Outline each Plasmodium ovale-infected red blood cell.
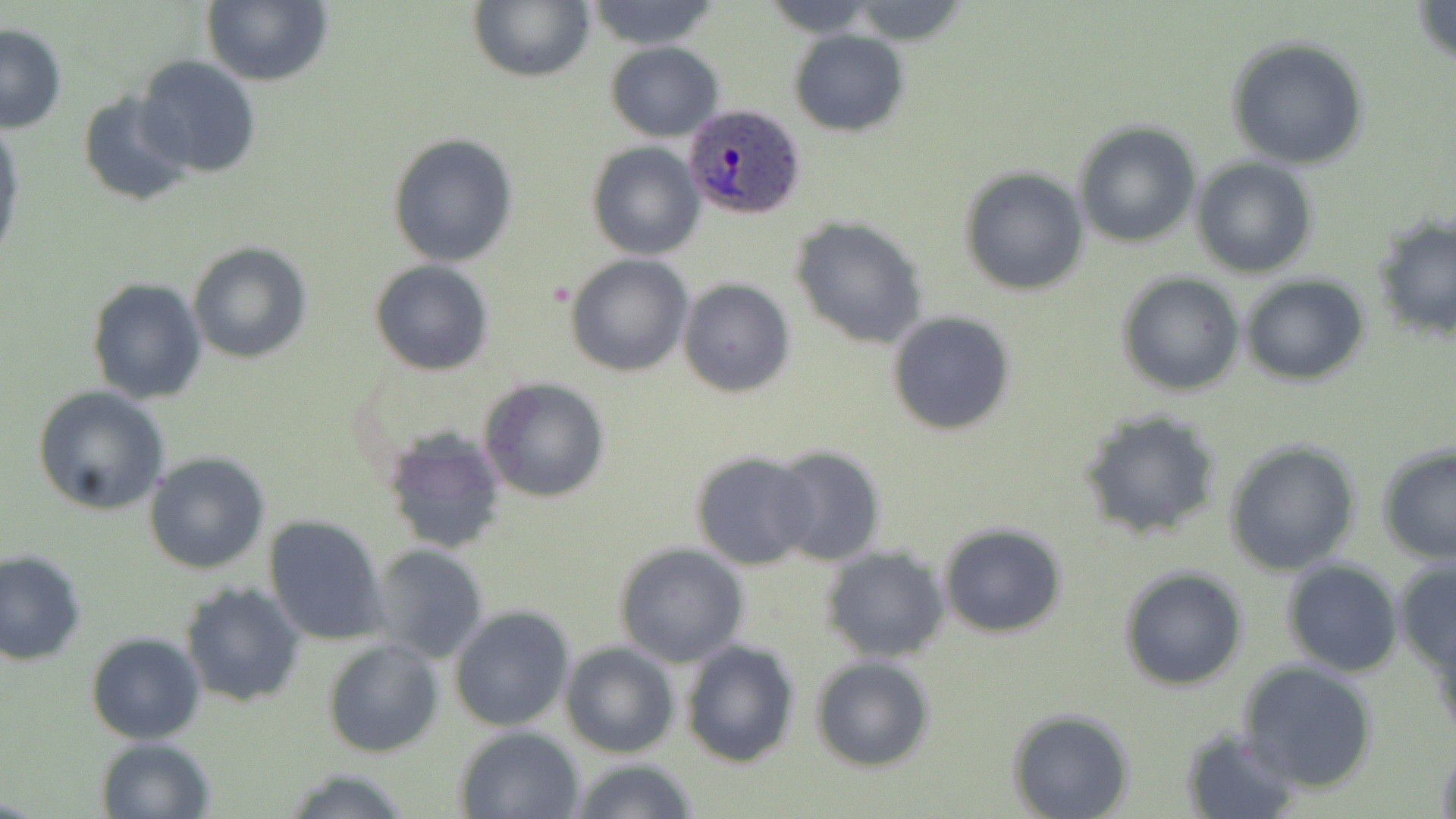
Approximate bounding boxes as [x1, y1, x2, y2] in pixels.
Plasmodium ovale-infected red blood cells: [681, 104, 808, 222].

Summary:
  - Uninfected red blood cell locations: [202, 0, 332, 88], [467, 1, 594, 83], [584, 1, 720, 50], [843, 1, 970, 45], [1412, 1, 1456, 67], [0, 22, 68, 132], [789, 30, 909, 136], [1225, 37, 1369, 170], [606, 41, 725, 141], [134, 55, 262, 178], [78, 90, 196, 207], [0, 121, 24, 266], [1073, 121, 1201, 248], [388, 133, 518, 267], [587, 142, 705, 259], [1192, 158, 1317, 278], [959, 166, 1091, 296], [1371, 212, 1456, 340], [790, 215, 927, 349], [188, 242, 312, 365], [565, 255, 692, 375], [370, 260, 493, 375], [1116, 272, 1244, 396], [1239, 275, 1369, 386], [87, 278, 208, 404], [677, 279, 797, 398], [885, 310, 1017, 437], [479, 378, 610, 503], [31, 385, 172, 517], [1077, 408, 1223, 539], [382, 429, 509, 554], [1225, 440, 1362, 576], [1375, 443, 1456, 564], [767, 444, 887, 567], [689, 451, 820, 570], [142, 452, 271, 575], [263, 515, 389, 646], [939, 524, 1068, 638], [613, 542, 748, 668], [370, 545, 489, 662], [822, 545, 950, 664], [0, 548, 87, 665], [1392, 558, 1456, 672], [1281, 560, 1402, 677], [1118, 566, 1247, 690], [178, 581, 306, 706], [449, 605, 575, 732], [1428, 621, 1456, 743], [86, 634, 206, 744], [322, 637, 444, 758], [680, 638, 802, 768], [559, 639, 680, 759], [810, 656, 936, 772], [1239, 661, 1380, 793], [1008, 710, 1134, 819], [454, 725, 586, 818], [1180, 729, 1302, 817], [95, 735, 219, 819], [1434, 741, 1456, 819], [566, 757, 699, 819], [278, 765, 417, 819]
  - Slide-level diagnosis: Plasmodium ovale
  - Image size: 1456×819 pixels
  - Modality: light microscopy
  - Magnification: 1000x
  - Stain: May-Grünwald-Giemsa
  - Preparation: thin blood film
  - Field of view: single